Name the parasite shown.
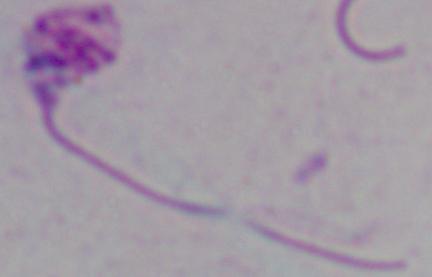
This is Leishmania.

Summary:
  - Magnification: 1000x
  - Modality: micrograph